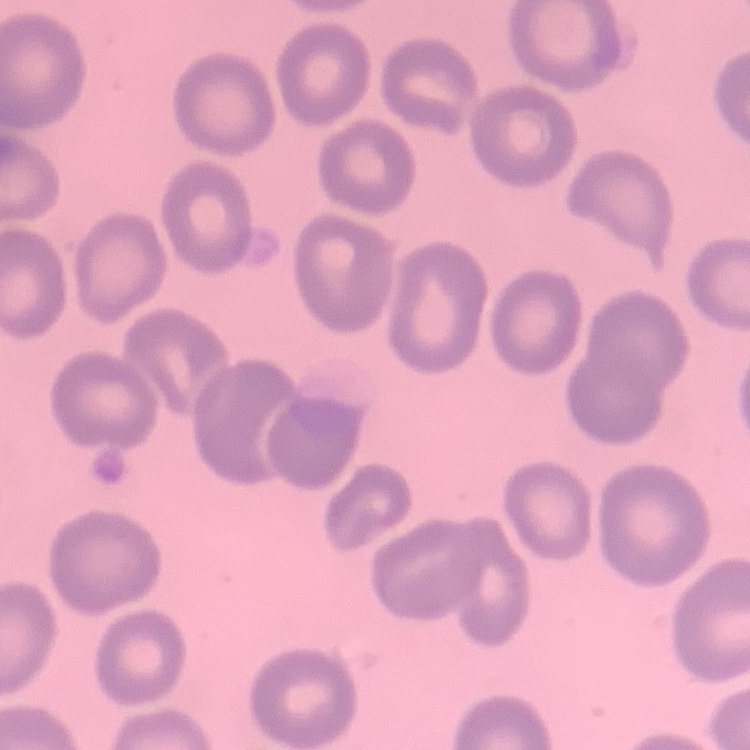

The red blood cells exhibit no rouleaux formation. One tile cut from a larger photomicrograph. Field's or Giemsa stain. Thin peripheral smear.